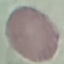

malaria status = uninfected
preparation = thin blood film
stain = Giemsa
image type = automatically extracted cell patch, resized to 64 × 64 pixels
capture = smartphone through the microscope eyepiece